Report the malaria status of this cell.
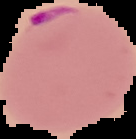

It is parasitized.

Summary:
  - Image type: segmented cell region on a black background
  - Image size: 136×139 pixels
  - Preparation: thin blood smear